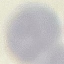

Summary:
  - Result: negative for malaria parasites
  - Capture: smartphone through the microscope eyepiece
  - Stain: Giemsa
  - Image type: automatically extracted cell patch, resized to 64 × 64 pixels
  - Preparation: thin smear